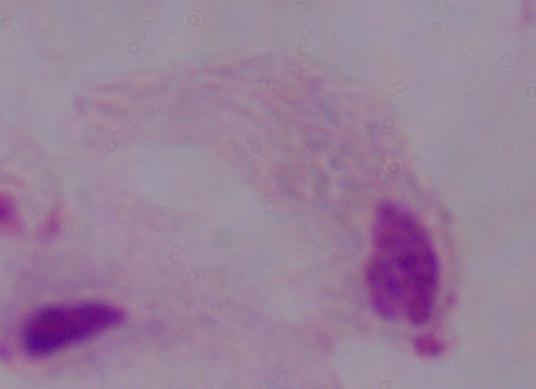
Micrograph. Captured at 1000x magnification. A trichomonad is shown.